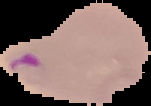
preparation = thin blood smear
image type = segmented cell region on a black background
malaria status = parasitized
image size = 151×106 pixels